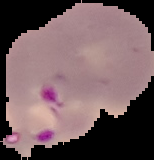
Malaria status: parasitized. From a thin blood film. Image is 154×160 pixels. The area outside the segmented cell region is set to black.